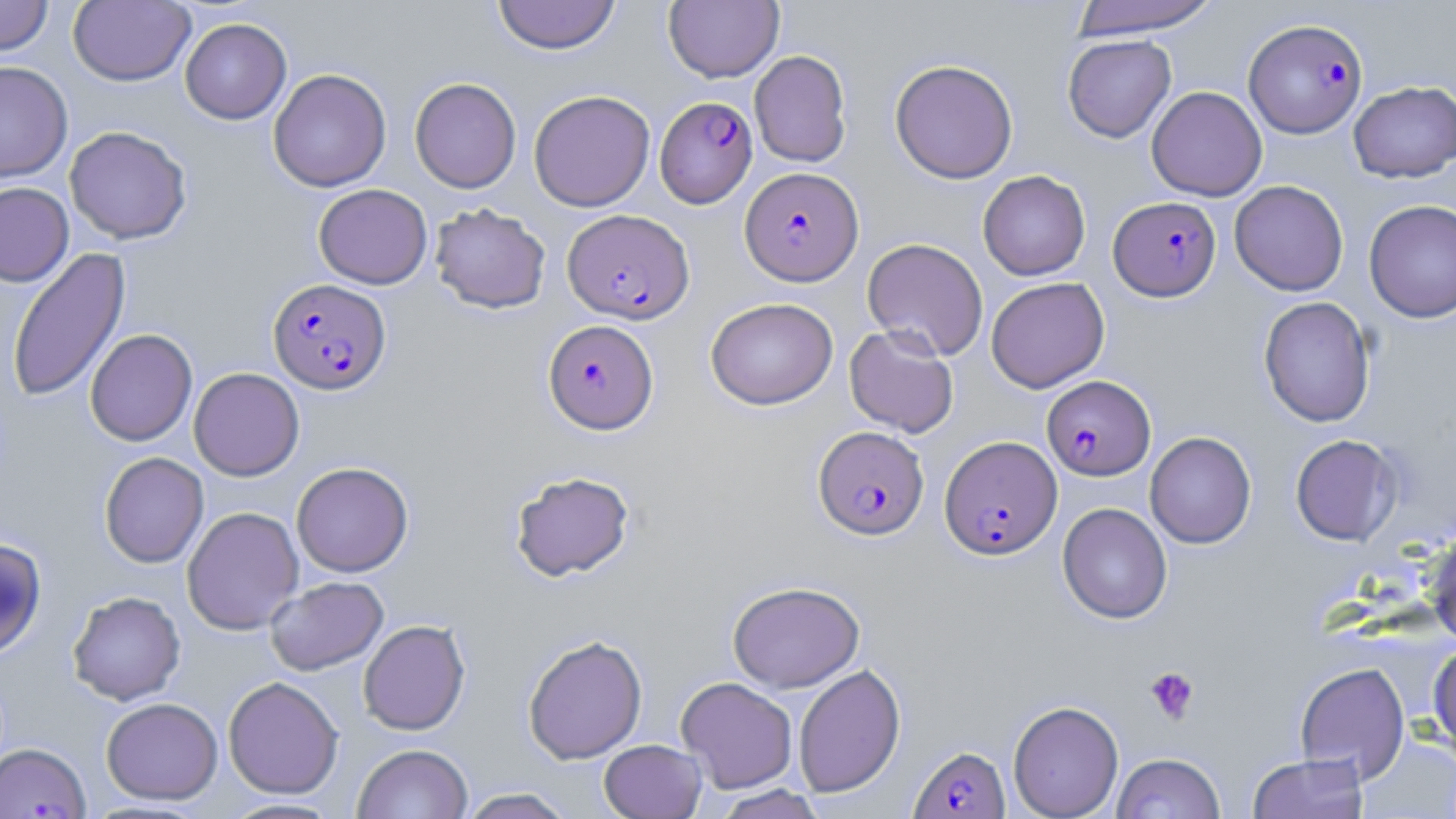

{
  "slide_level_diagnosis": "Plasmodium falciparum",
  "preparation": "thin blood film",
  "modality": "optical microscopy",
  "plasmodium_falciparum_infected_red_blood_cell_locations_subset": "approximate bounding boxes as (x1,y1)-(x2,y2) corner pairs in pixels: (1243,18)-(1368,138), (655,95)-(758,208), (740,167)-(863,284), (1109,196)-(1221,301), (563,208)-(694,324), (268,278)-(391,394), (544,319)-(658,433), (1042,375)-(1156,480), (813,425)-(928,540), (940,436)-(1062,559), (908,743)-(1010,819)",
  "stain": "May-Grünwald-Giemsa",
  "magnification": "1000x",
  "image_size": "1456×819 pixels",
  "field_of_view": "single",
  "uninfected_red_blood_cell_locations_subset": "approximate bounding boxes as (x1,y1)-(x2,y2) corner pairs in pixels: (0,0)-(54,56), (68,0)-(196,86), (492,0)-(620,55), (1067,0)-(1223,38), (664,1)-(783,83), (180,18)-(291,124), (1062,34)-(1176,143), (749,49)-(852,167), (890,59)-(1018,183), (0,61)-(73,182), (268,68)-(392,192), (409,77)-(521,193), (1348,80)-(1456,183), (1146,85)-(1267,201), (528,90)-(655,212), (64,126)-(192,245), (978,170)-(1090,280), (1229,180)-(1349,296), (0,182)-(74,287), (313,183)-(432,289), (1364,199)-(1456,323), (429,202)-(551,314), (862,238)-(989,360), (6,246)-(131,403), (986,277)-(1110,393), (1258,296)-(1376,427), (705,297)-(838,410), (844,325)-(959,438), (85,329)-(197,446), (188,367)-(304,481), (1144,431)-(1256,549), (1290,434)-(1403,546), (99,452)-(209,568), (291,462)-(413,577), (509,469)-(635,582), (1057,502)-(1173,623), (182,506)-(304,635), (1422,535)-(1456,644), (0,536)-(47,658), (265,576)-(388,676), (727,581)-(865,693), (67,590)-(186,705), (358,619)-(470,735), (523,633)-(647,764), (1428,642)-(1456,755), (1294,662)-(1410,781), (793,663)-(906,798), (223,676)-(344,799), (676,676)-(798,793), (101,697)-(223,804), (1008,700)-(1124,818), (1358,734)-(1456,818), (598,739)-(707,818), (352,743)-(473,818), (1111,752)-(1226,819), (1246,752)-(1369,819), (710,784)-(828,818), (456,787)-(577,818), (219,797)-(343,818)",
  "platelet_locations": "approximate bounding boxes as (x1,y1)-(x2,y2) corner pairs in pixels: (1145,667)-(1200,724)"
}